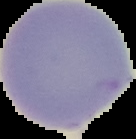

Summary:
  - Preparation: thin blood film
  - Image size: 136×139 pixels
  - Image type: segmented cell region on a black background
  - Malaria status: uninfected